Outline each uninfected red blood cell.
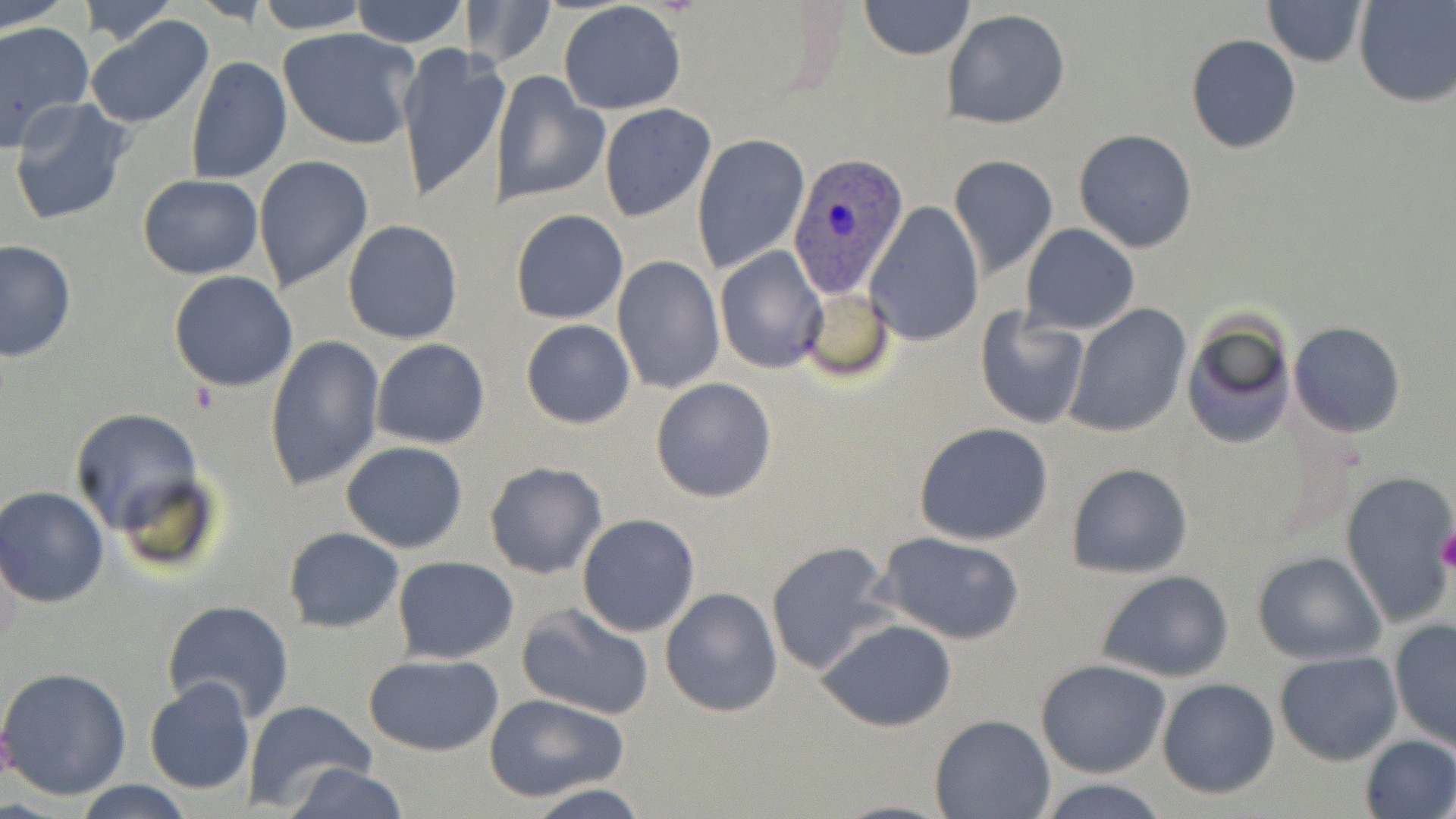

Approximate bounding boxes as named x1/y1/x2/y2 corners in pixels.
Uninfected red blood cells: (x1=2, y1=0, x2=71, y2=32), (x1=76, y1=0, x2=179, y2=46), (x1=252, y1=0, x2=372, y2=33), (x1=348, y1=0, x2=468, y2=49), (x1=1262, y1=0, x2=1370, y2=67), (x1=1353, y1=0, x2=1455, y2=107), (x1=859, y1=1, x2=974, y2=61), (x1=466, y1=2, x2=557, y2=72), (x1=557, y1=2, x2=688, y2=115), (x1=942, y1=9, x2=1072, y2=129), (x1=84, y1=15, x2=217, y2=129), (x1=0, y1=20, x2=93, y2=149), (x1=278, y1=27, x2=420, y2=150), (x1=1185, y1=34, x2=1302, y2=154), (x1=395, y1=42, x2=506, y2=206), (x1=186, y1=56, x2=291, y2=183), (x1=493, y1=71, x2=609, y2=206), (x1=8, y1=99, x2=132, y2=225), (x1=599, y1=103, x2=716, y2=221), (x1=1073, y1=128, x2=1199, y2=253), (x1=692, y1=135, x2=810, y2=274), (x1=949, y1=155, x2=1060, y2=279), (x1=255, y1=156, x2=373, y2=292), (x1=137, y1=174, x2=263, y2=280), (x1=867, y1=199, x2=984, y2=345), (x1=512, y1=208, x2=628, y2=324), (x1=342, y1=219, x2=463, y2=345), (x1=1020, y1=223, x2=1140, y2=334), (x1=0, y1=239, x2=76, y2=362), (x1=715, y1=247, x2=827, y2=376), (x1=611, y1=256, x2=723, y2=394), (x1=1038, y1=256, x2=1174, y2=403), (x1=168, y1=271, x2=297, y2=392), (x1=798, y1=287, x2=896, y2=382), (x1=1064, y1=302, x2=1191, y2=437), (x1=974, y1=308, x2=1090, y2=429), (x1=1180, y1=314, x2=1295, y2=451), (x1=521, y1=319, x2=636, y2=430), (x1=1290, y1=321, x2=1406, y2=436), (x1=263, y1=335, x2=383, y2=493), (x1=372, y1=338, x2=491, y2=450), (x1=650, y1=377, x2=777, y2=503), (x1=69, y1=407, x2=205, y2=539), (x1=914, y1=421, x2=1055, y2=544), (x1=339, y1=440, x2=469, y2=554), (x1=483, y1=460, x2=607, y2=579), (x1=1064, y1=462, x2=1194, y2=578), (x1=1340, y1=470, x2=1456, y2=627), (x1=1, y1=487, x2=111, y2=608), (x1=577, y1=513, x2=700, y2=638), (x1=283, y1=527, x2=404, y2=632), (x1=877, y1=531, x2=1026, y2=644), (x1=764, y1=540, x2=896, y2=677), (x1=1251, y1=551, x2=1385, y2=665), (x1=392, y1=555, x2=518, y2=665), (x1=1096, y1=569, x2=1234, y2=682), (x1=660, y1=587, x2=783, y2=718), (x1=162, y1=599, x2=295, y2=723), (x1=517, y1=601, x2=655, y2=721), (x1=818, y1=619, x2=957, y2=732), (x1=1389, y1=619, x2=1455, y2=751), (x1=1274, y1=650, x2=1403, y2=765), (x1=362, y1=653, x2=504, y2=755), (x1=1036, y1=659, x2=1170, y2=777), (x1=0, y1=666, x2=132, y2=800), (x1=144, y1=677, x2=255, y2=796), (x1=1157, y1=677, x2=1280, y2=799), (x1=485, y1=693, x2=629, y2=802), (x1=242, y1=701, x2=377, y2=813), (x1=929, y1=713, x2=1055, y2=818), (x1=1359, y1=734, x2=1456, y2=818), (x1=280, y1=762, x2=410, y2=819), (x1=1033, y1=778, x2=1174, y2=817), (x1=71, y1=780, x2=195, y2=819), (x1=525, y1=786, x2=650, y2=818).

{
  "slide_level_diagnosis": "Plasmodium ovale",
  "field_of_view": "one of a larger specimen",
  "platelet_locations": "approximate bounding boxes as named x1/y1/x2/y2 corners in pixels: (x1=1438, y1=529, x2=1456, y2=573)",
  "stain": "May-Grünwald-Giemsa",
  "modality": "light microscopy",
  "magnification": "1000x",
  "preparation": "thin blood film",
  "plasmodium_ovale_infected_red_blood_cell_locations": "approximate bounding boxes as named x1/y1/x2/y2 corners in pixels: (x1=788, y1=153, x2=911, y2=296)",
  "image_size": "1456×819 pixels"
}